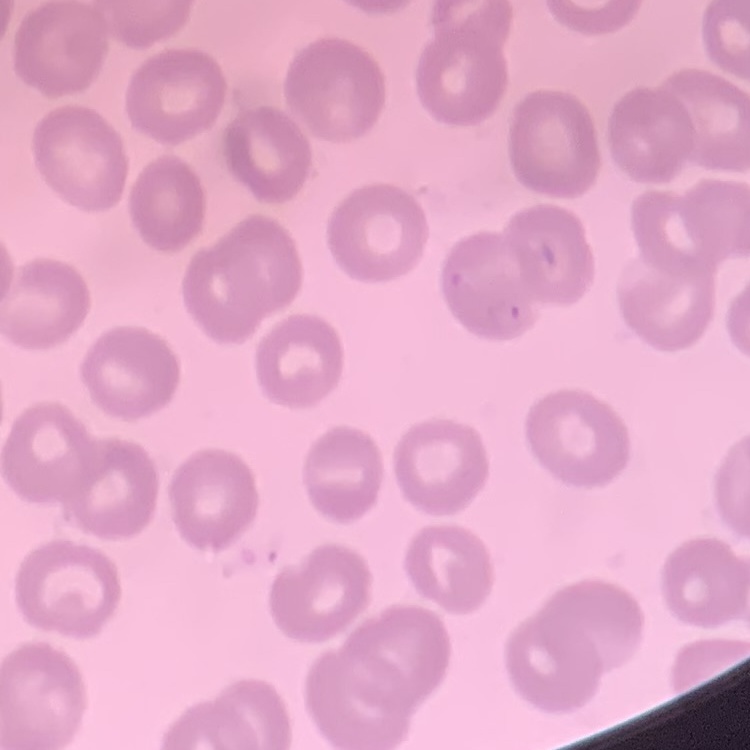

red blood cell morphology = no rouleaux formation
preparation = thin blood smear
image type = square crop of a larger photomicrograph
stain = Field's or Giemsa